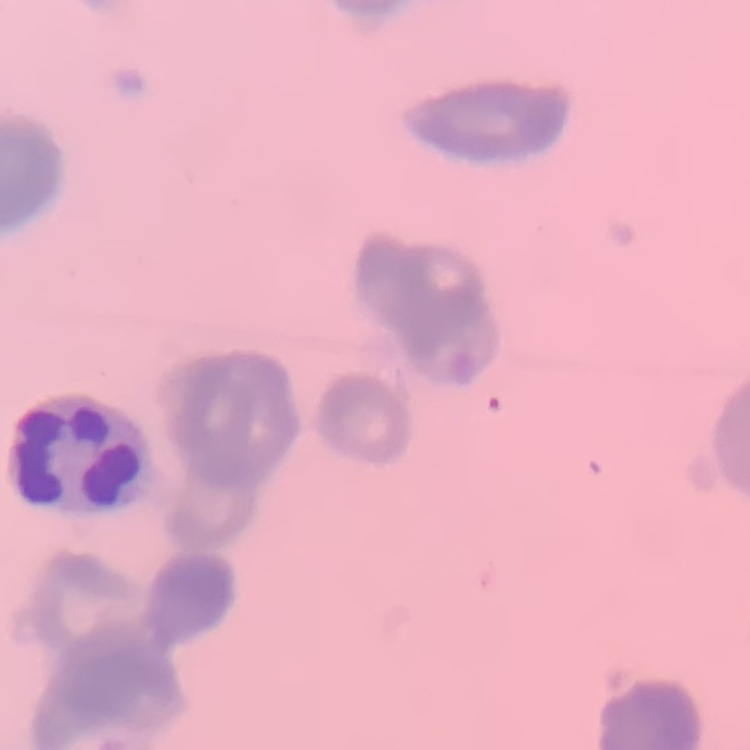
erythrocyte_morphology: rouleaux formation
image_type: square crop of a larger photomicrograph
preparation: thin peripheral smear
stain: Field's or Giemsa